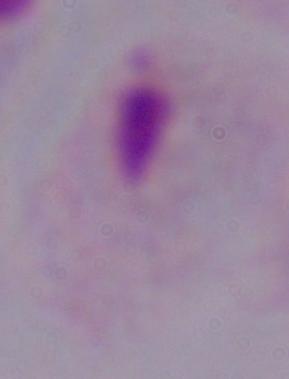

Summary:
  - Modality: photomicrograph
  - Identification: trichomonad
  - Magnification: 1000x